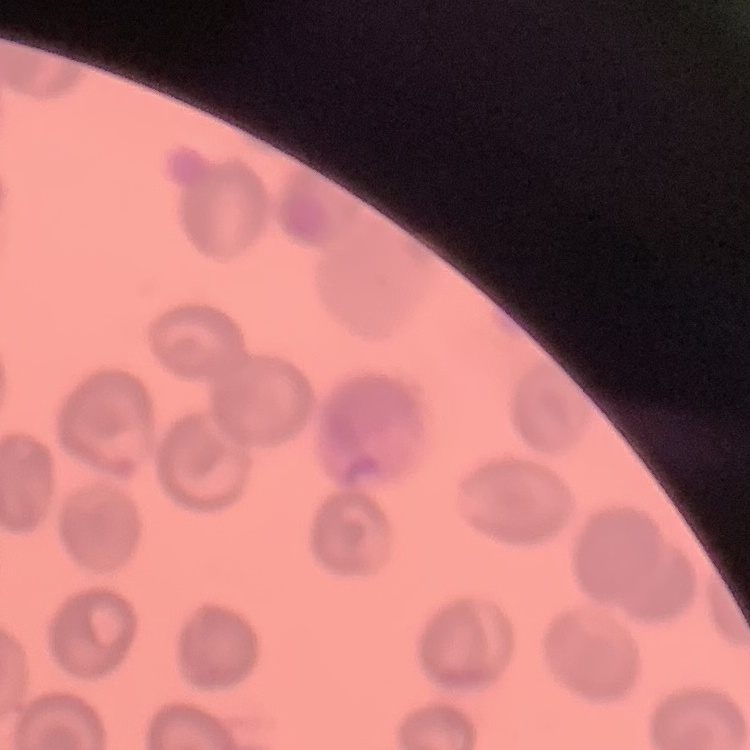 The erythrocytes show no rouleaux formation. Square crop of a larger photomicrograph. Field's or Giemsa stain. Thin blood smear.